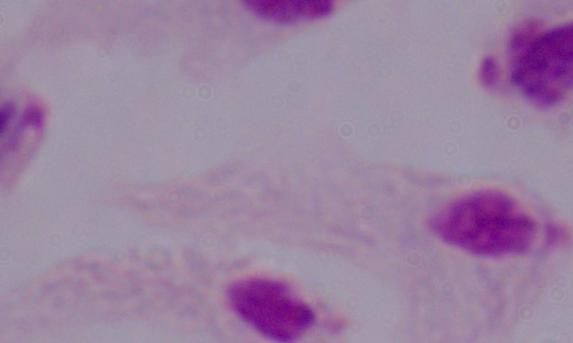
Summary:
  - Magnification: 1000x
  - Modality: micrograph
  - Identification: trichomonad